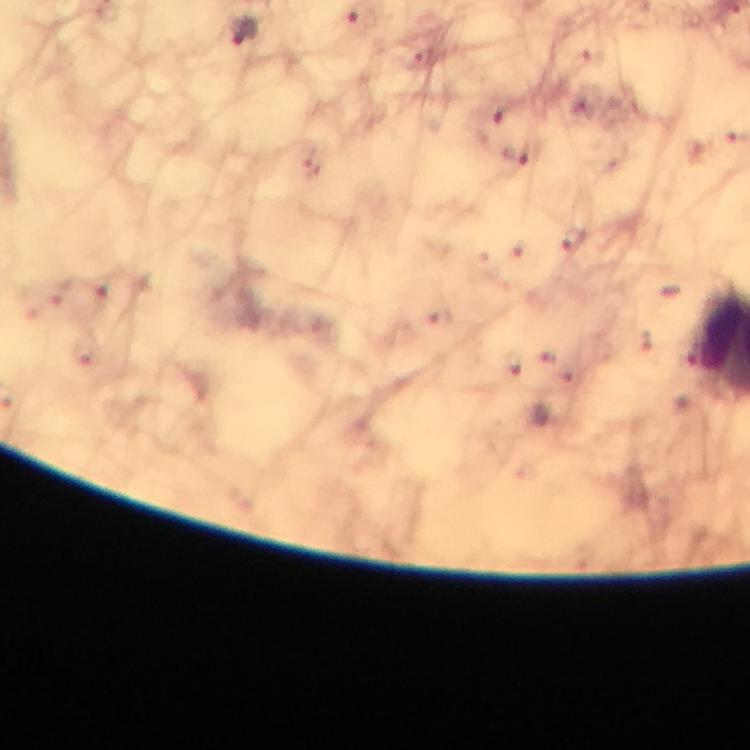

Approximate centers as [x, y] in pixels. Malaria parasite locations: [244, 31], [496, 116], [516, 154]. From a diagnostic examination for malaria. Cropped region of a single field of view. 100x magnification. Thick blood smear. Immersion oil was used. Photographed with a smartphone mounted on the microscope. Image is 750×750 pixels. Giemsa stain.